Name the parasite shown.
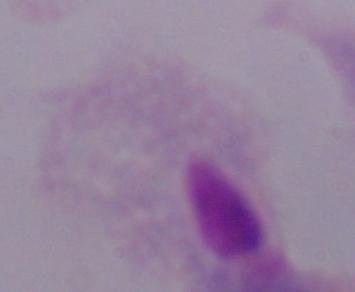

A trichomonad.

Photomicrograph. 1000x magnification.